Outline each Plasmodium ovale-infected red blood cell.
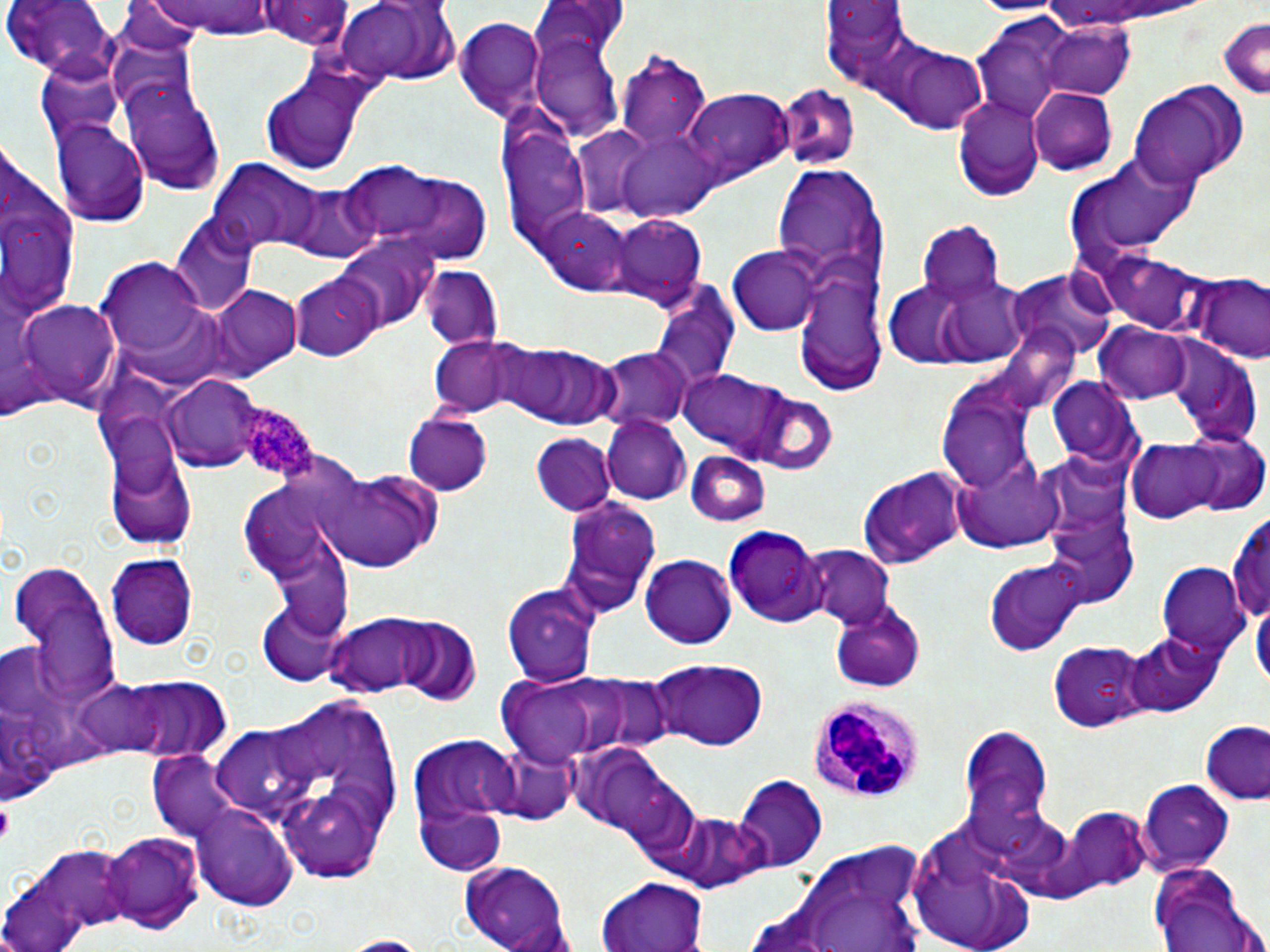

Approximate bounding boxes as (x1,y1)-(x2,y2) corner pairs in pixels.
Plasmodium ovale-infected red blood cells: (235,400)-(317,482).

Uninfected red blood cell locations: (3,0)-(117,78), (141,0)-(291,36), (261,0)-(352,48), (327,1)-(448,86), (530,1)-(630,74), (1028,1)-(1212,33), (824,6)-(912,89), (456,18)-(547,119), (1215,19)-(1270,100), (970,20)-(1069,118), (1040,22)-(1135,100), (532,28)-(626,141), (894,47)-(991,133), (617,55)-(715,154), (39,57)-(125,146), (253,62)-(379,177), (121,77)-(226,194), (1129,80)-(1246,186), (774,85)-(858,170), (1027,89)-(1117,175), (683,90)-(792,187), (951,95)-(1044,200), (52,118)-(151,228), (503,124)-(593,249), (616,124)-(722,226), (1081,153)-(1203,253), (207,157)-(334,256), (336,161)-(450,246), (773,166)-(885,292), (369,167)-(496,265), (279,181)-(378,260), (541,208)-(634,292), (606,214)-(706,309), (170,216)-(256,315), (920,219)-(1002,301), (334,233)-(438,333), (728,245)-(820,336), (1097,248)-(1213,339), (101,260)-(206,359), (793,260)-(887,395), (422,265)-(503,351), (1007,267)-(1115,359), (292,272)-(384,363), (1192,278)-(1268,365), (211,284)-(302,378), (651,288)-(740,400), (887,288)-(968,367), (20,300)-(121,411), (121,302)-(243,392), (1095,324)-(1196,403), (428,335)-(524,417), (496,341)-(618,428), (1166,346)-(1262,447), (599,349)-(692,431), (682,369)-(786,453), (166,373)-(265,472), (936,374)-(1043,495), (1048,378)-(1143,468), (744,388)-(838,475), (403,413)-(493,496), (601,414)-(691,505), (1164,429)-(1267,516), (532,434)-(615,515), (1127,436)-(1232,523), (682,451)-(770,527), (107,453)-(196,550), (957,456)-(1064,551), (316,463)-(443,571), (858,467)-(965,568), (556,496)-(662,615), (1044,501)-(1140,607), (1228,509)-(1269,629), (722,526)-(827,628), (265,532)-(354,643), (638,543)-(812,639), (803,547)-(894,629), (105,554)-(196,652), (982,555)-(1086,656), (642,556)-(735,650), (6,559)-(120,703), (1157,564)-(1250,657), (506,583)-(599,687), (258,599)-(352,684), (830,600)-(927,693), (1250,601)-(1269,693), (331,612)-(442,694), (393,619)-(481,704), (1126,630)-(1223,717), (1050,641)-(1153,732), (651,658)-(767,749), (557,674)-(678,759), (76,675)-(169,763), (499,678)-(605,762), (119,679)-(227,758), (247,698)-(410,884), (1197,721)-(1270,805), (959,724)-(1055,840), (411,740)-(516,866), (569,741)-(689,846), (488,742)-(576,823), (146,749)-(243,844), (731,776)-(828,870), (1137,780)-(1234,872), (192,803)-(298,910), (1063,809)-(1154,892), (664,812)-(771,894), (905,820)-(1039,952), (102,832)-(203,934), (792,843)-(931,951), (9,847)-(139,944), (457,860)-(574,951), (1150,860)-(1263,952), (599,875)-(709,952), (0,880)-(90,952), (337,934)-(429,951). Platelet locations: (0,802)-(13,840). White blood cell locations: (808,694)-(924,804). Slide-level diagnosis: Plasmodium ovale. 1000x magnification. Optical microscopy. Thin blood film. One field of a larger specimen. May-Grünwald-Giemsa stain. Image is 1270×952 pixels.